Assess this cell for malaria.
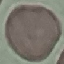

It is uninfected.

Summary:
  - Stain: Giemsa
  - Capture: smartphone camera at the microscope eyepiece
  - Preparation: thin smear
  - Image type: automatically extracted cell patch, resized to 64 × 64 pixels